State which parasite is depicted.
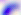
This is Toxoplasma gondii.

{
  "magnification": "400x",
  "modality": "photomicrograph"
}